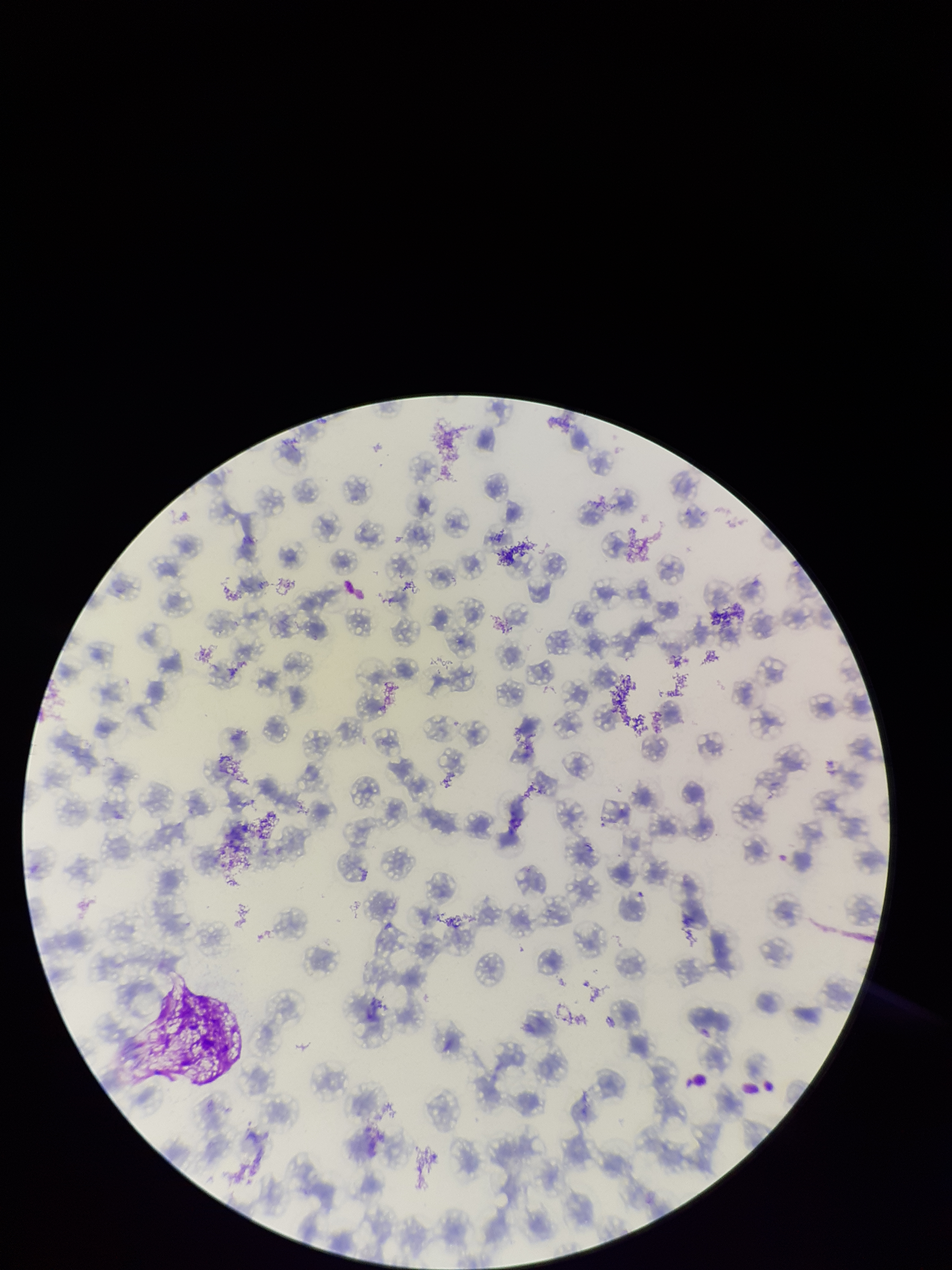
species reported for this patient = Plasmodium falciparum
preparation = thin blood smear
parasitized red blood cells = none detected
patient malaria status = infected
field of view = single
parasitized red blood cell count = 0
red blood cell count = 108
stain = Giemsa
capture = smartphone photograph through the microscope eyepiece
image size = 952×1270 pixels